Point out each malaria parasite and classify it by life-cycle stage.
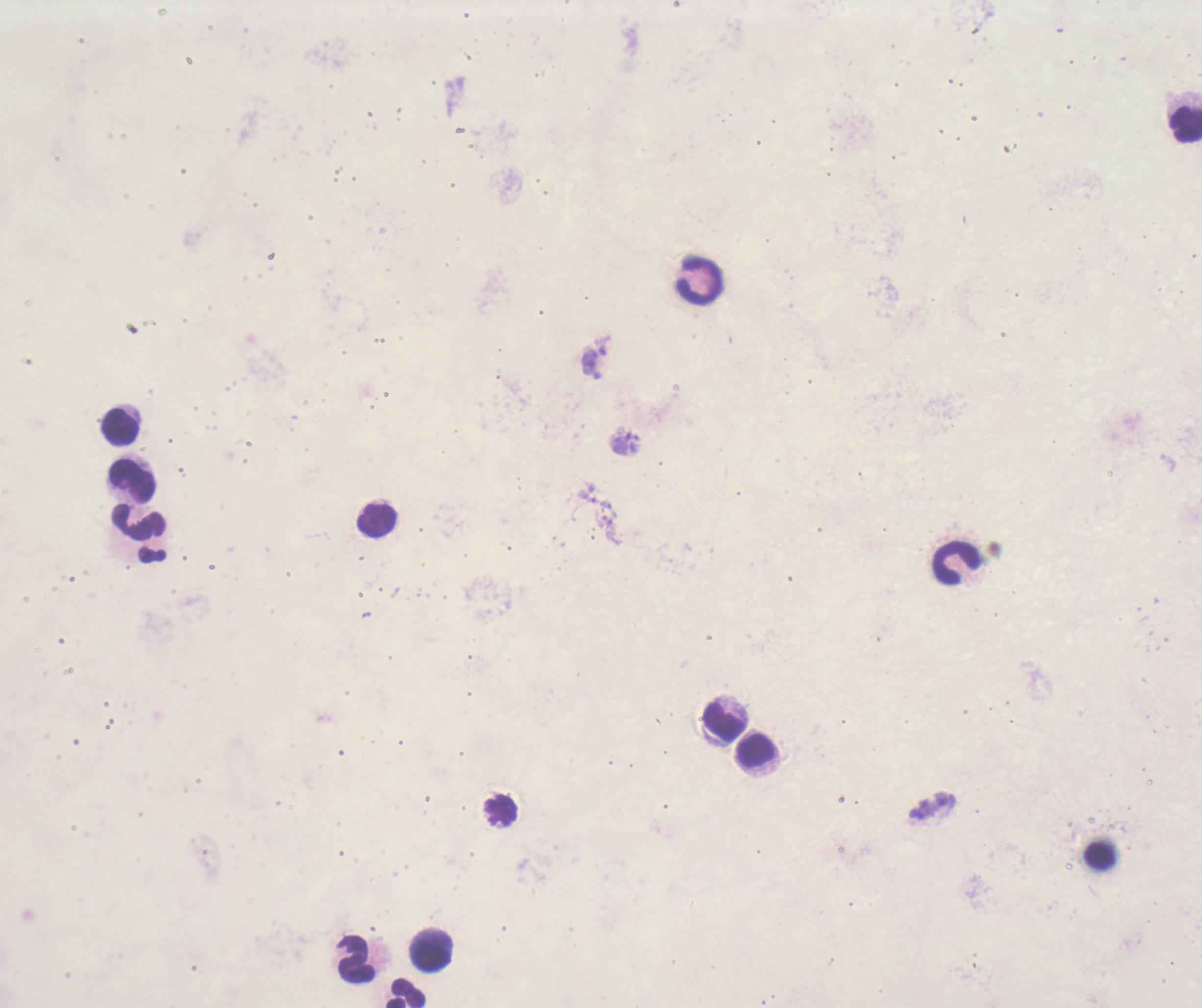
No malaria parasites seen.

Approximate centers as [x, y] in pixels. Leukocyte locations: [1184, 124], [700, 280], [121, 428], [131, 480], [376, 518], [137, 524], [956, 562], [722, 720], [756, 749], [502, 811], [1100, 855], [431, 950], [355, 961], [405, 994]. Single field of view. Captured at 100x magnification. Romanowsky stain. Previously used in an actual diagnosis. Background quality: poor. Coloration quality: bad. Thick smear of blood. Image is 1202×1008 pixels.